Classify this cell by malaria status.
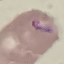

Parasitized.

Automatically extracted cell patch, resized to 64 × 64 pixels. Thin blood film. Giemsa-stained preparation. Photographed with a smartphone camera at the microscope eyepiece.